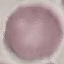
Summary:
  - Result: no malaria parasites seen
  - Capture: smartphone through the microscope eyepiece
  - Image type: automatically extracted cell patch, resized to 64 × 64 pixels
  - Stain: Giemsa
  - Preparation: thin blood film